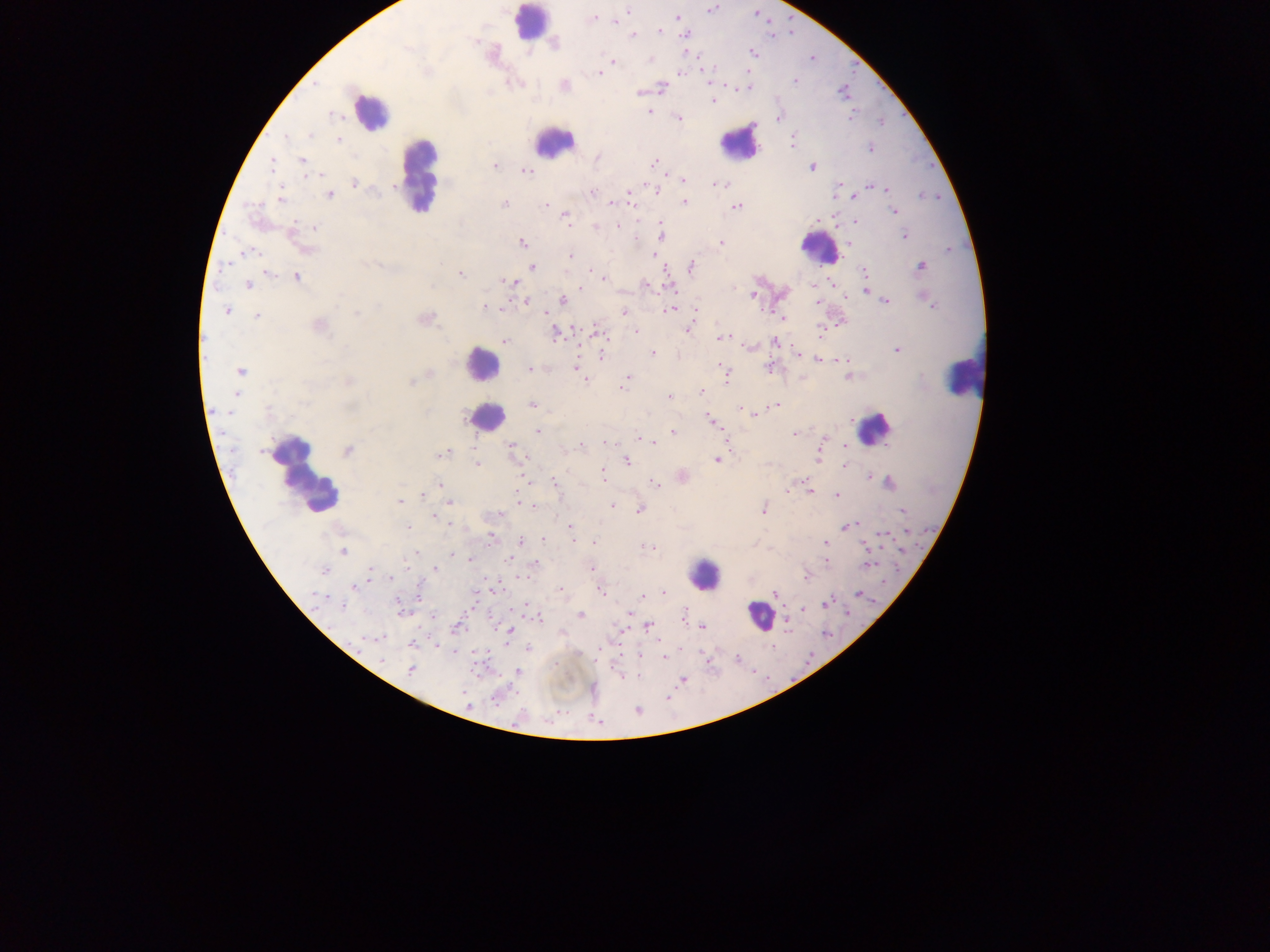
Approximate centers as [x, y] in pixels. Plasmodium parasite locations: [710, 8], [628, 11], [678, 18], [591, 19], [617, 22], [659, 31], [684, 32], [631, 34], [750, 52], [685, 53], [650, 59], [612, 61], [598, 72], [680, 72], [796, 81], [563, 85], [748, 86], [661, 88], [639, 91], [712, 100], [648, 112], [778, 117], [679, 118], [337, 139], [791, 142], [870, 148], [597, 157], [302, 161], [655, 162], [495, 165], [811, 167], [525, 170], [682, 179], [353, 183], [869, 186], [657, 190], [885, 190], [591, 192], [630, 192], [836, 192], [329, 194], [854, 195], [281, 198], [631, 198], [684, 201], [504, 204], [545, 204], [611, 204], [736, 205], [895, 212], [565, 216], [854, 220], [817, 221], [616, 225], [314, 227], [595, 227], [291, 234], [660, 235], [904, 235], [521, 241], [849, 242], [720, 243], [306, 249], [246, 253], [657, 255], [569, 257], [532, 266], [921, 266], [689, 267], [268, 272], [863, 272], [460, 274], [596, 274], [297, 276], [603, 278], [511, 282], [249, 284], [645, 284], [832, 284], [668, 286], [583, 288], [866, 289], [751, 295], [843, 296], [927, 299], [526, 300], [561, 300], [886, 302], [486, 307], [670, 309], [226, 310], [544, 312], [623, 312], [695, 312], [776, 314], [257, 315], [781, 318], [424, 319], [839, 321], [318, 325], [687, 329], [636, 330], [821, 331], [597, 332], [557, 333], [722, 338], [505, 341], [775, 341], [748, 347], [897, 349], [652, 353], [796, 354], [601, 357], [817, 359], [838, 359], [770, 366], [529, 369], [577, 369], [722, 369], [240, 371], [725, 373], [849, 376], [627, 378], [411, 381], [624, 389], [700, 392], [236, 395], [669, 397], [533, 405], [775, 405], [740, 409], [754, 415], [711, 422], [538, 432], [673, 432], [794, 434], [638, 439], [645, 439], [726, 439], [823, 439], [654, 441], [604, 442], [582, 445], [512, 446], [843, 447], [347, 450], [441, 454], [819, 457], [625, 460], [717, 460], [477, 465], [844, 465], [602, 474], [681, 476], [868, 476], [804, 481], [888, 482], [655, 484], [440, 485], [787, 487], [807, 489], [423, 495], [837, 496], [399, 502], [448, 502], [519, 503], [612, 505], [638, 508], [763, 508], [901, 511], [433, 516], [847, 526], [408, 528], [569, 528], [908, 531], [881, 534], [490, 536], [543, 538], [519, 541], [823, 542], [593, 543], [863, 545], [652, 547], [902, 549], [343, 551], [415, 552], [450, 553], [472, 559], [510, 559], [825, 561], [535, 563], [867, 565], [433, 568], [590, 568], [323, 570], [369, 572], [805, 575], [355, 586], [561, 589], [492, 590], [601, 590], [662, 592], [858, 593], [418, 594], [774, 594], [641, 597], [826, 602], [526, 607], [803, 608], [402, 613], [630, 614], [432, 615], [580, 615], [683, 615], [637, 618], [785, 620], [647, 625], [703, 626], [456, 627], [623, 630], [509, 631], [377, 638], [436, 643], [411, 644], [528, 647], [638, 655], [663, 655], [410, 669], [519, 671], [621, 677], [682, 679], [466, 703]. Leukocyte locations: [530, 24], [369, 112], [739, 142], [552, 143], [420, 173], [819, 247], [481, 364], [963, 376], [485, 417], [875, 429], [304, 474], [702, 575], [759, 616]. Thick blood film. One field of view. Image is 1270×952 pixels. Mobile-phone photograph taken through the microscope. Sample from Ghana.